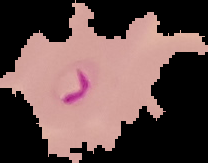

Summary:
  - Result: Plasmodium parasites identified
  - Image type: cell region segmented out of the field of view; surrounding area masked to black
  - Preparation: thin blood smear
  - Image size: 208×163 pixels